Classify this cell by malaria status.
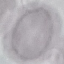

Uninfected.

preparation: thin blood smear
stain: Giemsa
capture: smartphone camera at the microscope eyepiece
image_type: automatically extracted cell patch, resized to 64 × 64 pixels